Identify the preparation type.
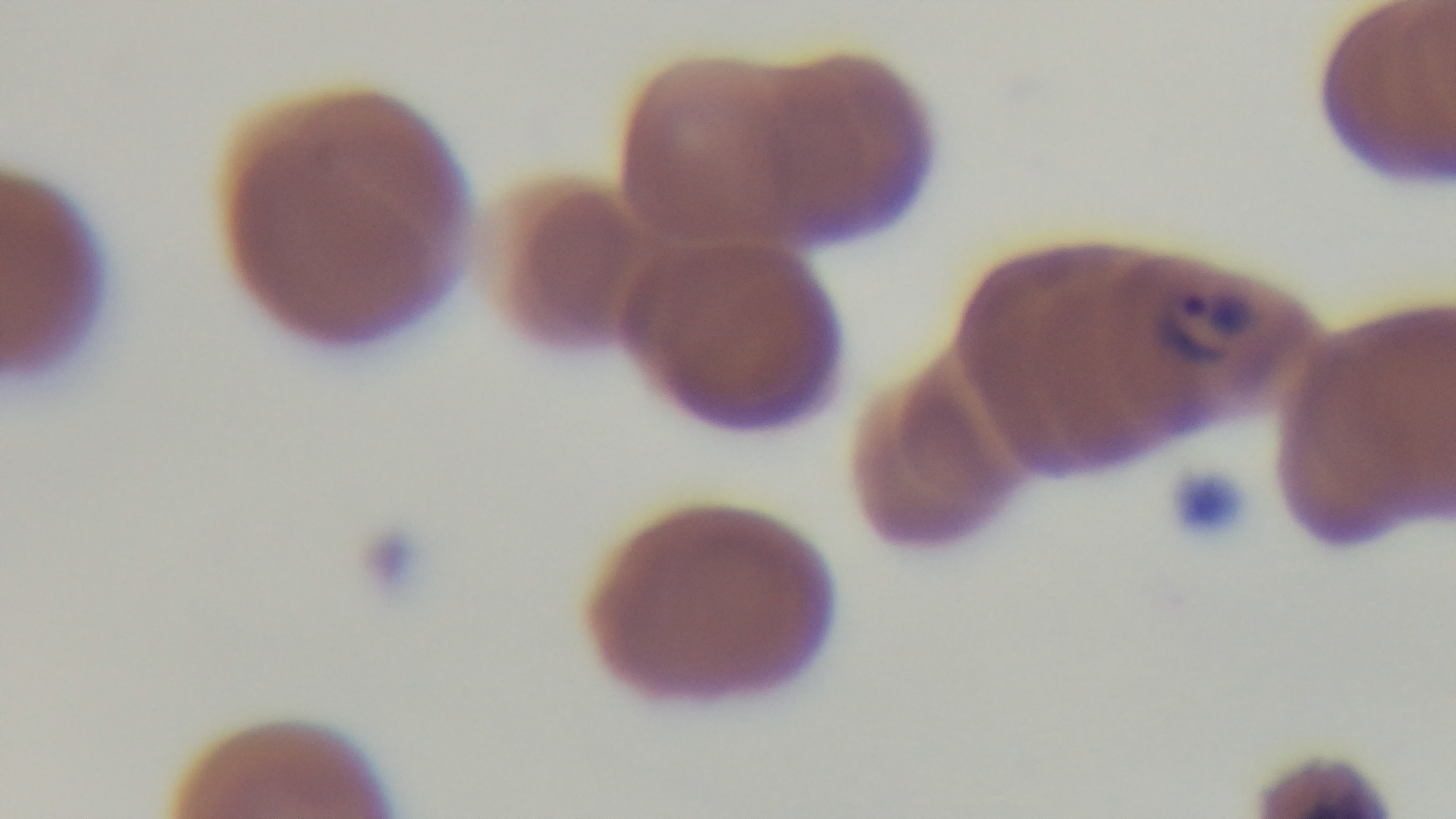

It is a thin blood film.

Summary:
  - Stain: Giemsa
  - Objective: 100x oil immersion
  - Modality: light microscopy
  - Field of view: single
  - Malaria status: infected
  - Capture: mounted 4K digital camera